Assess the morphology of the erythrocytes.
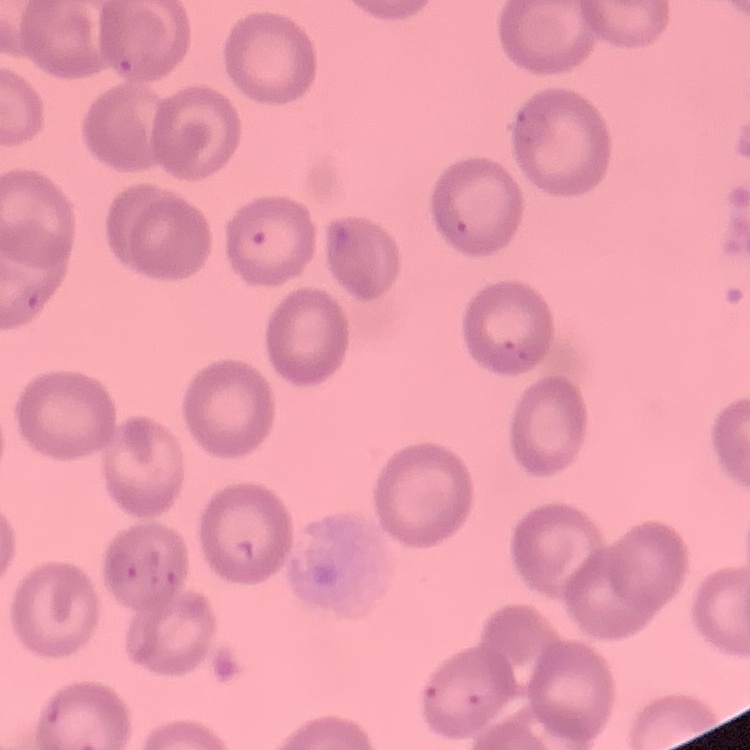

They show no rouleaux formation.

Summary:
  - Preparation: thin peripheral smear
  - Stain: Field's or Giemsa
  - Image type: one tile cut from a larger photomicrograph